Assess this cell for malaria.
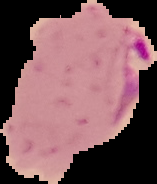

Parasitized.

Summary:
  - Image type: segmented cell region on a black background
  - Preparation: thin blood film
  - Image size: 157×184 pixels